Classify this cell by malaria status.
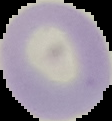
It is uninfected.

Image is 112×121 pixels. The area outside the segmented cell region is set to black. From a thin blood smear.